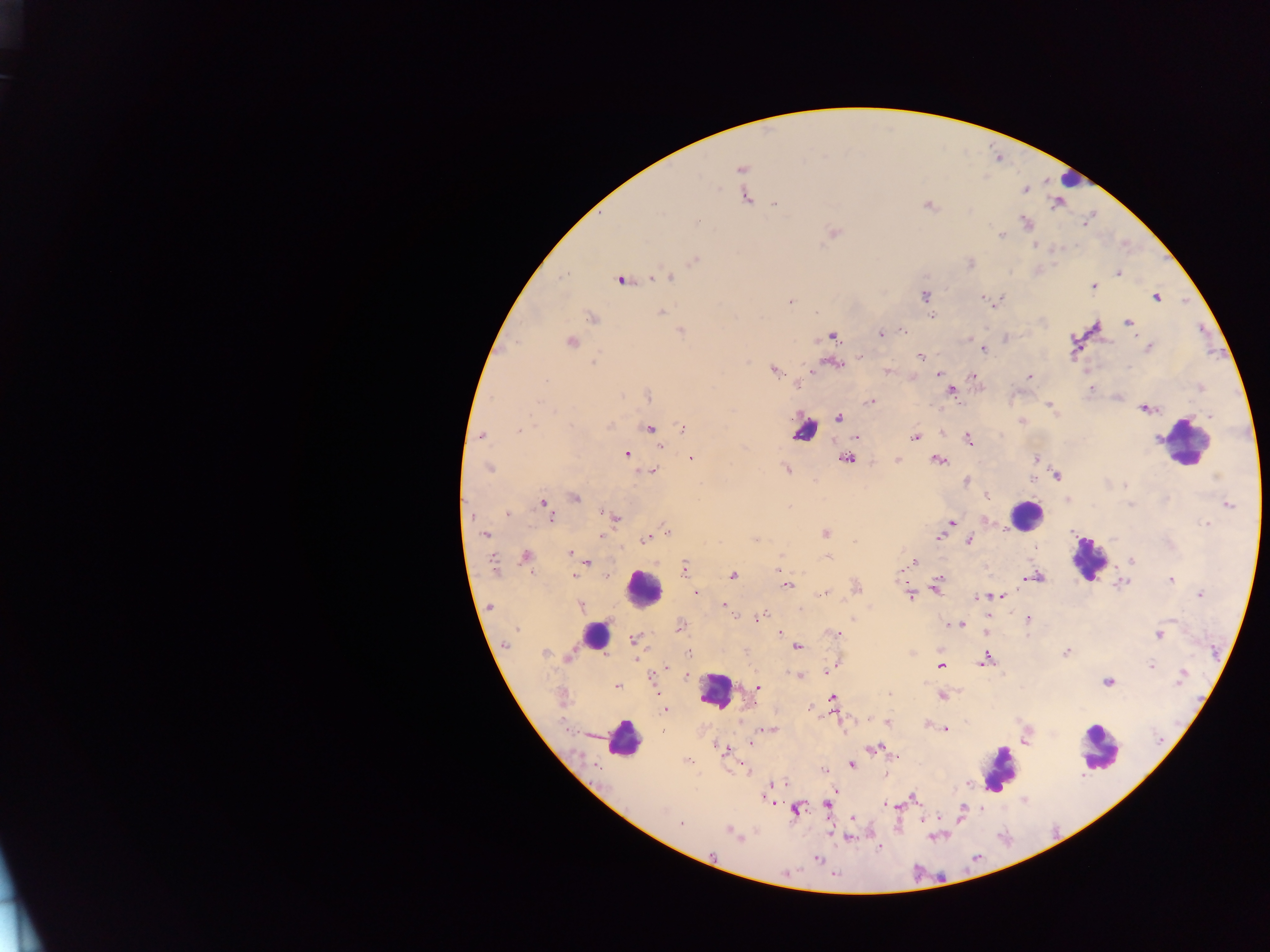

preparation: thick blood film
malaria_parasite_locations: 'approximate centers as [x, y] in pixels: [826, 154], [805, 161], [741, 171], [748, 197], [774, 203], [926, 205], [1054, 205], [696, 221], [1024, 223], [834, 233], [1000, 235], [1034, 245], [1054, 250], [694, 260], [971, 263], [1117, 274], [671, 276], [650, 279], [622, 280], [1093, 287], [1156, 296], [925, 297], [981, 298], [789, 301], [661, 311], [591, 318], [1129, 322], [1097, 328], [902, 330], [1200, 330], [680, 331], [881, 333], [833, 336], [1073, 338], [570, 342], [1147, 347], [983, 351], [860, 355], [921, 356], [856, 359], [593, 360], [1130, 368], [886, 370], [774, 371], [938, 374], [972, 376], [1028, 376], [797, 382], [1091, 388], [951, 390], [648, 396], [871, 402], [1049, 404], [1142, 409], [1053, 411], [1208, 415], [839, 417], [1020, 420], [610, 424], [518, 429], [682, 429], [650, 430], [481, 436], [856, 438], [913, 438], [969, 439], [1157, 439], [661, 448], [627, 455], [691, 457], [847, 458], [1036, 459], [898, 460], [940, 461], [488, 468], [788, 470], [652, 472], [1058, 475], [1216, 477], [1032, 479], [967, 480], [1124, 485], [575, 497], [987, 497], [1066, 498], [544, 503], [1130, 504], [1230, 504], [508, 511], [471, 516], [552, 519], [615, 519], [986, 520], [951, 522], [667, 532], [826, 533], [484, 535], [940, 535], [602, 536], [756, 537], [644, 540], [853, 540], [969, 542], [1033, 547], [570, 552], [901, 554], [526, 555], [827, 556], [916, 561], [1132, 561], [496, 562], [589, 563], [686, 566], [778, 567], [1039, 574], [575, 576], [734, 576], [899, 577], [1043, 577], [1028, 578], [1169, 580], [1121, 583], [1127, 584], [786, 585], [937, 586], [696, 591], [935, 591], [823, 594], [1198, 594], [911, 597], [982, 597], [1004, 597], [580, 605], [723, 606], [489, 607], [800, 608], [757, 618], [1028, 618], [949, 623], [961, 623], [779, 631], [833, 634], [1160, 636], [633, 640], [505, 647], [797, 647], [912, 652], [1065, 652], [545, 653], [986, 653], [687, 654], [568, 657], [984, 660], [980, 662], [1152, 664], [942, 667], [1183, 671], [827, 672], [798, 676], [687, 677], [1107, 681], [1181, 683], [615, 686], [758, 687], [889, 694], [942, 695], [831, 697], [810, 708], [664, 710], [559, 718], [886, 720], [946, 728], [768, 730], [748, 742], [715, 743], [719, 748], [873, 749], [727, 752], [895, 756], [686, 760], [851, 766], [748, 772], [773, 781], [968, 786], [834, 792], [913, 797], [917, 800], [771, 803], [827, 806], [886, 806], [896, 807], [962, 809], [797, 810], [853, 818], [680, 823], [847, 837], [738, 838], [816, 860]'
leukocyte_locations: 'approximate centers as [x, y] in pixels: [1066, 177], [809, 425], [1187, 443], [1025, 516], [1093, 565], [641, 589], [595, 642], [710, 696], [623, 745], [1099, 753], [1003, 767]'
field_of_view: single
capture: mobile-phone photograph through a microscope
image_size: 1270×952 pixels
country: Ghana